Look for Plasmodium parasites.
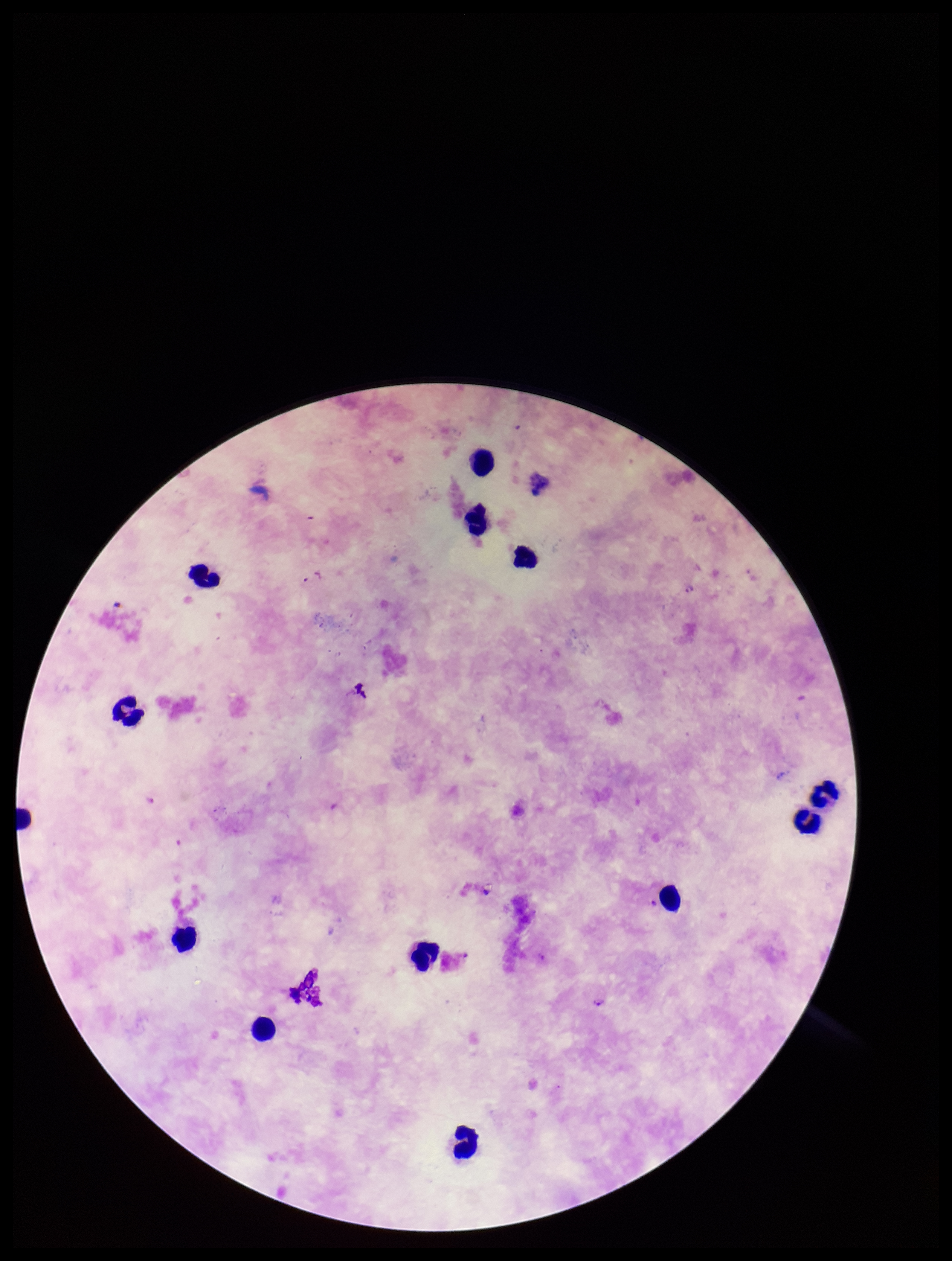
Identified.

image size = 952×1261 pixels
parasite count = 2
patient malaria status = infected
field of view = one from this slide
stain = Giemsa
species reported for this patient = Plasmodium falciparum
leukocyte count = 14
capture = smartphone photograph through the microscope eyepiece
preparation = thick smear